Classify this cell by malaria status.
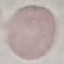

Uninfected.

stain: Giemsa
preparation: thin smear
image_type: cell patch, automatically extracted from a larger field of view and resized to 64 × 64 pixels
capture: smartphone through the microscope eyepiece